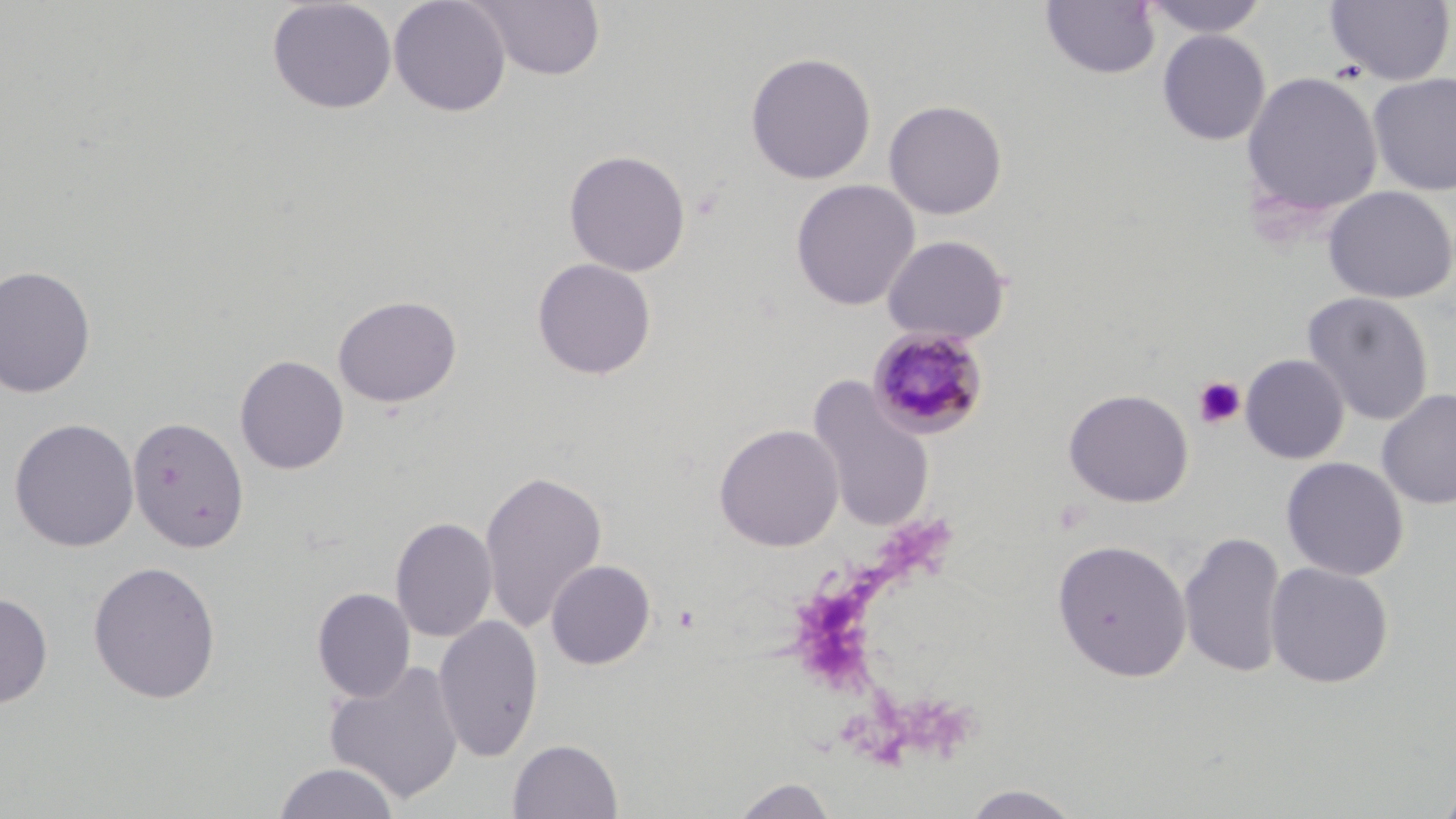

slide-level diagnosis = Plasmodium malariae
magnification = 1000x
uninfected red blood cell locations = approximate bounding boxes as (x1,y1)-(x2,y2) corner pairs in pixels: (266,0)-(397,115), (388,0)-(511,117), (471,0)-(606,82), (1040,0)-(1161,79), (1141,0)-(1271,39), (1324,1)-(1455,86), (1157,29)-(1271,145), (745,51)-(876,185), (1241,70)-(1384,221), (1367,72)-(1456,196), (883,99)-(1008,220), (563,149)-(691,276), (790,179)-(920,311), (1322,185)-(1456,304), (881,234)-(1011,345), (532,257)-(657,380), (0,264)-(96,398), (1301,291)-(1434,425), (332,295)-(462,408), (1240,353)-(1349,464), (234,354)-(349,475), (806,377)-(935,531), (1063,388)-(1194,508), (1377,388)-(1455,509), (127,415)-(250,554), (9,417)-(140,552), (713,423)-(845,552), (1281,456)-(1409,581), (479,467)-(608,634), (390,515)-(498,643), (1179,529)-(1288,680), (1053,538)-(1192,682), (87,560)-(222,705), (545,560)-(656,670), (1265,561)-(1394,688), (312,588)-(416,702), (0,591)-(53,708), (434,614)-(545,763), (323,659)-(466,806), (507,739)-(624,819), (272,761)-(402,819), (1436,772)-(1456,819), (728,775)-(841,818), (958,784)-(1086,819)
platelet locations = approximate bounding boxes as (x1,y1)-(x2,y2) corner pairs in pixels: (1193,376)-(1246,430), (673,604)-(702,634)
modality = light microscopy
stain = May-Grünwald-Giemsa
field of view = single
image size = 1456×819 pixels
preparation = thin blood smear
Plasmodium malariae-infected red blood cell locations = approximate bounding boxes as (x1,y1)-(x2,y2) corner pairs in pixels: (867,326)-(989,440)